Assess this cell for malaria.
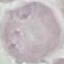

It is uninfected.

stain: Giemsa
image_type: automatically extracted cell patch, resized to 64 × 64 pixels
preparation: thin blood film
capture: smartphone through the microscope eyepiece